Comment on the morphology of the erythrocytes.
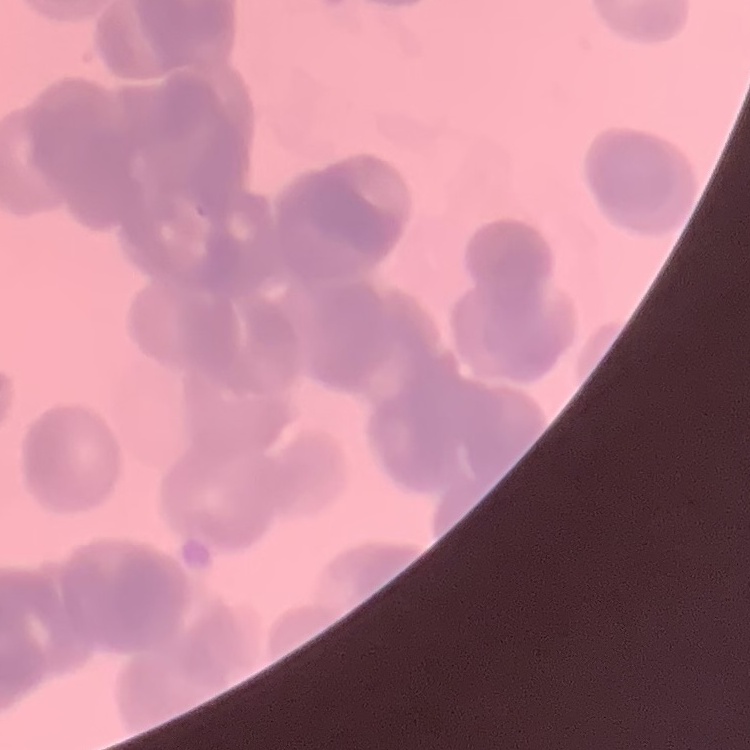

They show rouleaux formation.

stain = Field's or Giemsa
image type = square crop of a larger photomicrograph
preparation = thin peripheral smear